Describe the morphology of the erythrocytes.
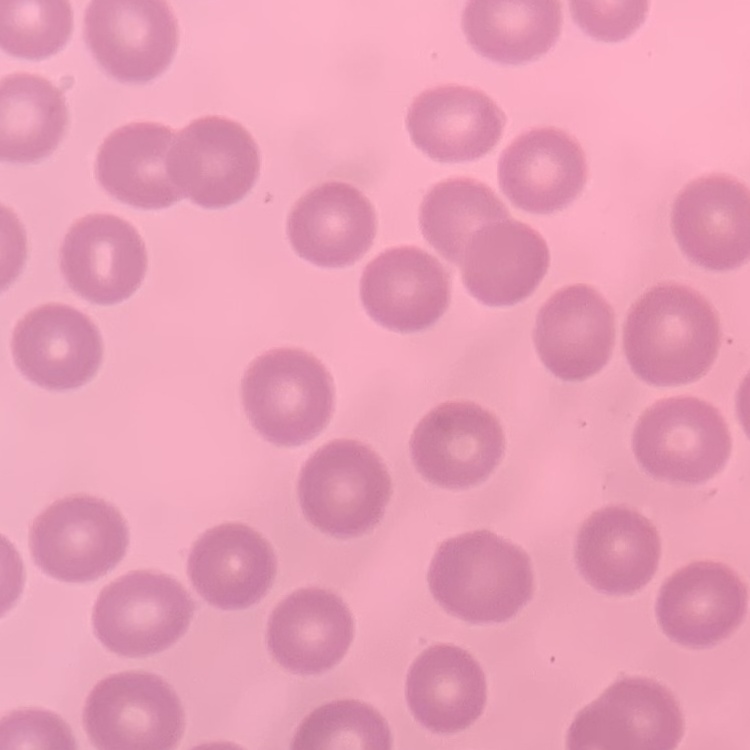
No rouleaux formation.

Thin blood smear. Field's or Giemsa stain. One tile cut from a larger photomicrograph.